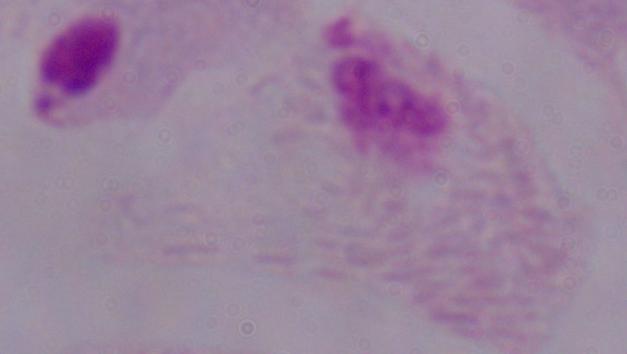
magnification = 1000x
modality = micrograph
identification = trichomonad